Classify this cell by malaria status.
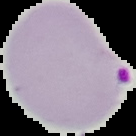

It is parasitized.

image_type: segmented cell region on a black background
image_size: 136×136 pixels
preparation: thin blood film